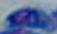

Summary:
  - Modality: micrograph
  - Identification: Toxoplasma gondii
  - Magnification: 1000x